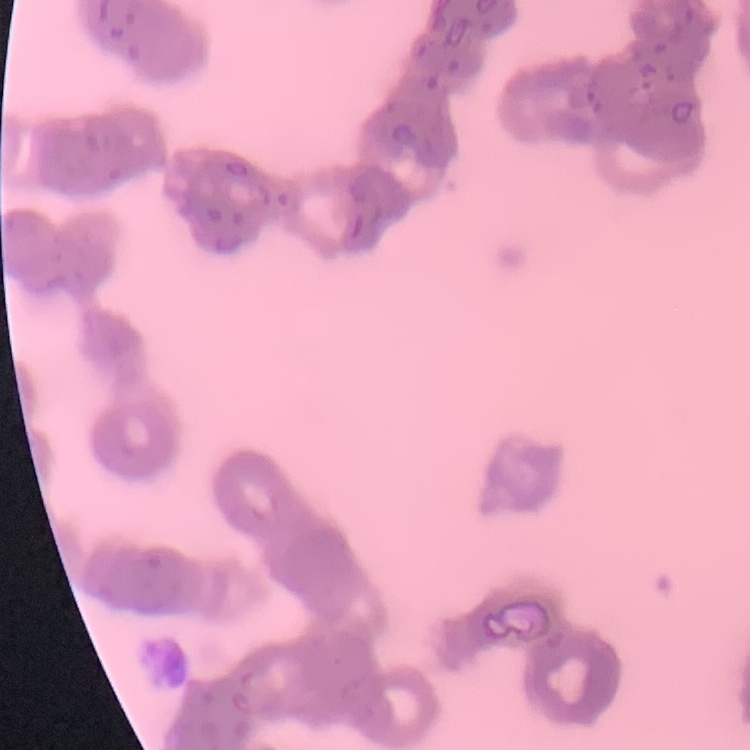
{
  "erythrocyte_morphology": "rouleaux formation",
  "preparation": "thin blood film",
  "image_type": "one tile cut from a larger photomicrograph",
  "stain": "Field's or Giemsa"
}